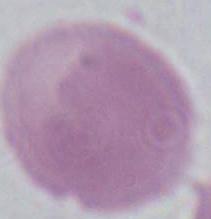

Summary:
  - Identification: red blood cell
  - Modality: micrograph
  - Magnification: 1000x